Report the malaria status of this cell.
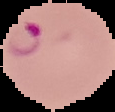

Parasitized.

The area outside the segmented cell region is set to black. From a thin blood film. Image is 115×112 pixels.